Report the malaria status of this cell.
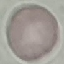

It is uninfected.

Summary:
  - Image type: automatically extracted cell patch, resized to 64 × 64 pixels
  - Capture: smartphone through the microscope eyepiece
  - Preparation: thin blood film
  - Stain: Giemsa